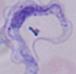
Summary:
  - Identification: trypanosome
  - Magnification: 1000x
  - Modality: micrograph